State which parasite is depicted.
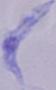
This is a trypanosome.

Micrograph. 1000x magnification.